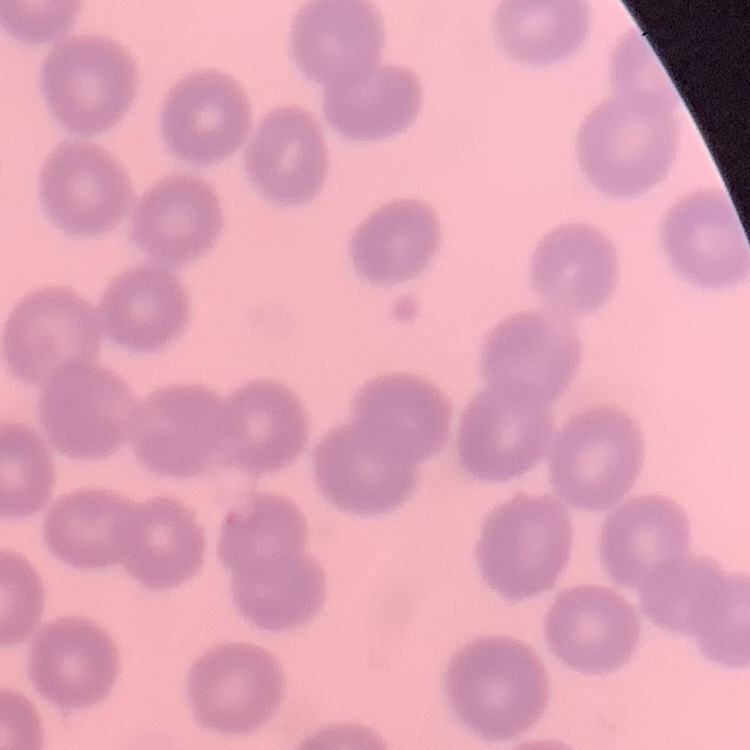
red_blood_cell_morphology: no rouleaux formation
image_type: one tile cut from a larger photomicrograph
stain: Field's or Giemsa
preparation: thin peripheral smear